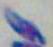

Toxoplasma gondii is shown. 1000x magnification. Photomicrograph.